Locate every Plasmodium falciparum-infected red blood cell.
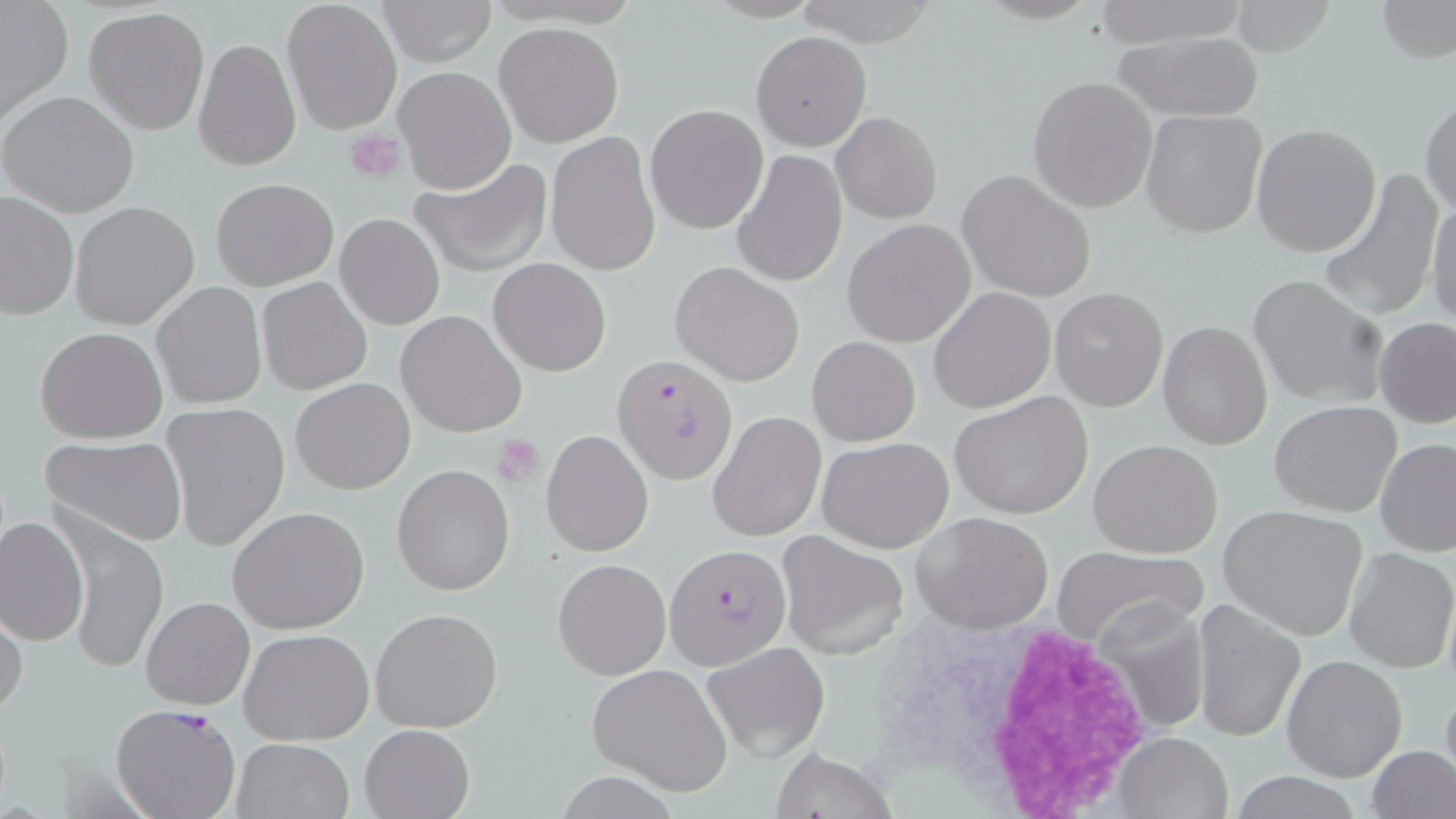

Approximate bounding boxes as [x1, y1, x2, y2] in pixels.
Plasmodium falciparum-infected red blood cells: [613, 356, 735, 484], [665, 544, 791, 667], [112, 703, 241, 819].

slide-level diagnosis = Plasmodium falciparum
image size = 1456×819 pixels
uninfected red blood cell locations = approximate bounding boxes as [x1, y1, x2, y2] in pixels: [377, 0, 497, 66], [793, 0, 940, 47], [1091, 0, 1251, 46], [1375, 0, 1454, 62], [281, 1, 401, 136], [0, 2, 73, 122], [84, 7, 210, 136], [494, 21, 623, 148], [750, 31, 871, 151], [1112, 31, 1265, 121], [193, 36, 301, 172], [393, 64, 517, 193], [1029, 76, 1158, 214], [1, 91, 139, 216], [1420, 91, 1456, 220], [644, 102, 767, 233], [829, 109, 941, 223], [1142, 109, 1267, 238], [1251, 123, 1381, 257], [545, 132, 660, 275], [733, 148, 848, 288], [409, 155, 554, 277], [1320, 166, 1446, 321], [957, 170, 1096, 302], [212, 178, 338, 290], [0, 190, 79, 320], [1429, 194, 1456, 332], [70, 201, 200, 330], [336, 213, 444, 329], [843, 220, 975, 348], [489, 258, 611, 377], [671, 261, 804, 386], [1247, 275, 1387, 408], [257, 277, 373, 395], [153, 282, 266, 408], [1049, 286, 1169, 411], [927, 287, 1056, 413], [397, 310, 527, 437], [1375, 318, 1456, 428], [1158, 320, 1272, 450], [36, 328, 168, 444], [808, 336, 920, 447], [755, 360, 869, 497], [290, 377, 415, 494], [950, 391, 1095, 519], [1270, 400, 1400, 516], [161, 403, 291, 551], [709, 411, 825, 541], [542, 430, 653, 556], [41, 435, 188, 548], [818, 437, 953, 553], [1376, 437, 1456, 556], [1089, 438, 1223, 557], [391, 464, 515, 595], [228, 506, 371, 632], [1219, 506, 1369, 640], [911, 512, 1055, 633], [1, 513, 88, 648], [65, 521, 166, 675], [776, 532, 912, 661], [1050, 544, 1208, 648], [1345, 548, 1456, 674], [553, 558, 672, 680], [141, 596, 254, 709], [1193, 603, 1303, 743], [1094, 604, 1211, 736], [371, 606, 504, 733], [0, 607, 27, 722], [240, 628, 373, 746], [704, 644, 830, 760], [1282, 655, 1407, 783], [588, 662, 735, 797], [1440, 674, 1456, 787], [359, 724, 475, 819], [1112, 732, 1234, 819], [231, 737, 357, 819], [1368, 745, 1456, 819], [769, 749, 897, 818], [1229, 773, 1365, 818]
stain = May-Grünwald-Giemsa
platelet locations = approximate bounding boxes as [x1, y1, x2, y2] in pixels: [345, 130, 406, 181], [492, 435, 546, 485]
field of view = one of a larger specimen
modality = light microscopy
white blood cell locations = approximate bounding boxes as [x1, y1, x2, y2] in pixels: [868, 604, 1165, 816]
magnification = 1000x
preparation = thin blood smear